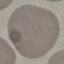
malaria status = uninfected
preparation = thin blood film
stain = Giemsa
capture = smartphone camera at the microscope eyepiece
image type = cell patch, automatically extracted from a larger field of view and resized to 64 × 64 pixels